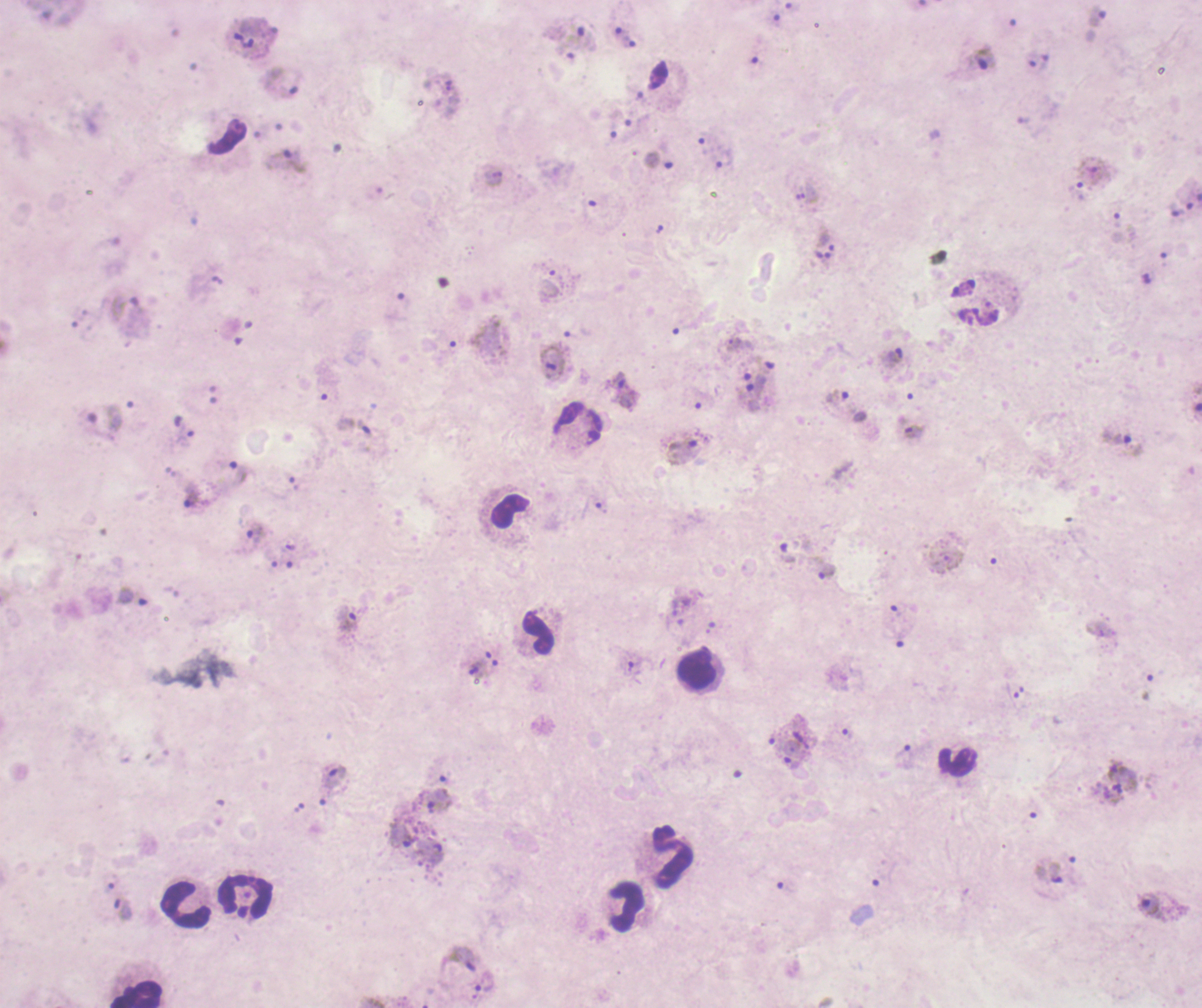
image_size: 1202×1008 pixels
field_of_view: single
stain: Romanowsky
context: previously used in a real diagnosis
trophozoite_locations: 'approximate centers as (x, y) in pixels: (1097, 17), (586, 39), (628, 44), (984, 59), (1044, 62), (721, 159), (291, 160), (891, 360), (553, 361), (623, 391), (105, 420), (914, 432), (1116, 437), (682, 452), (239, 471), (195, 498), (255, 536), (787, 552), (825, 572), (132, 596), (346, 620), (898, 638), (478, 669), (904, 752), (790, 756), (1121, 772), (332, 776), (436, 800), (400, 833), (435, 853), (1047, 872), (1148, 905), (121, 909), (463, 959)'
preparation: thick smear of blood
leukocyte_locations: 'approximate centers as (x, y) in pixels: (579, 425), (510, 513), (540, 632), (696, 667), (957, 761), (672, 856), (244, 896), (186, 905), (625, 907), (136, 995)'
result: positive for Plasmodium parasites
coloration_quality: bad
magnification: 100x
background_quality: poor